Outline each Plasmodium malariae-infected red blood cell.
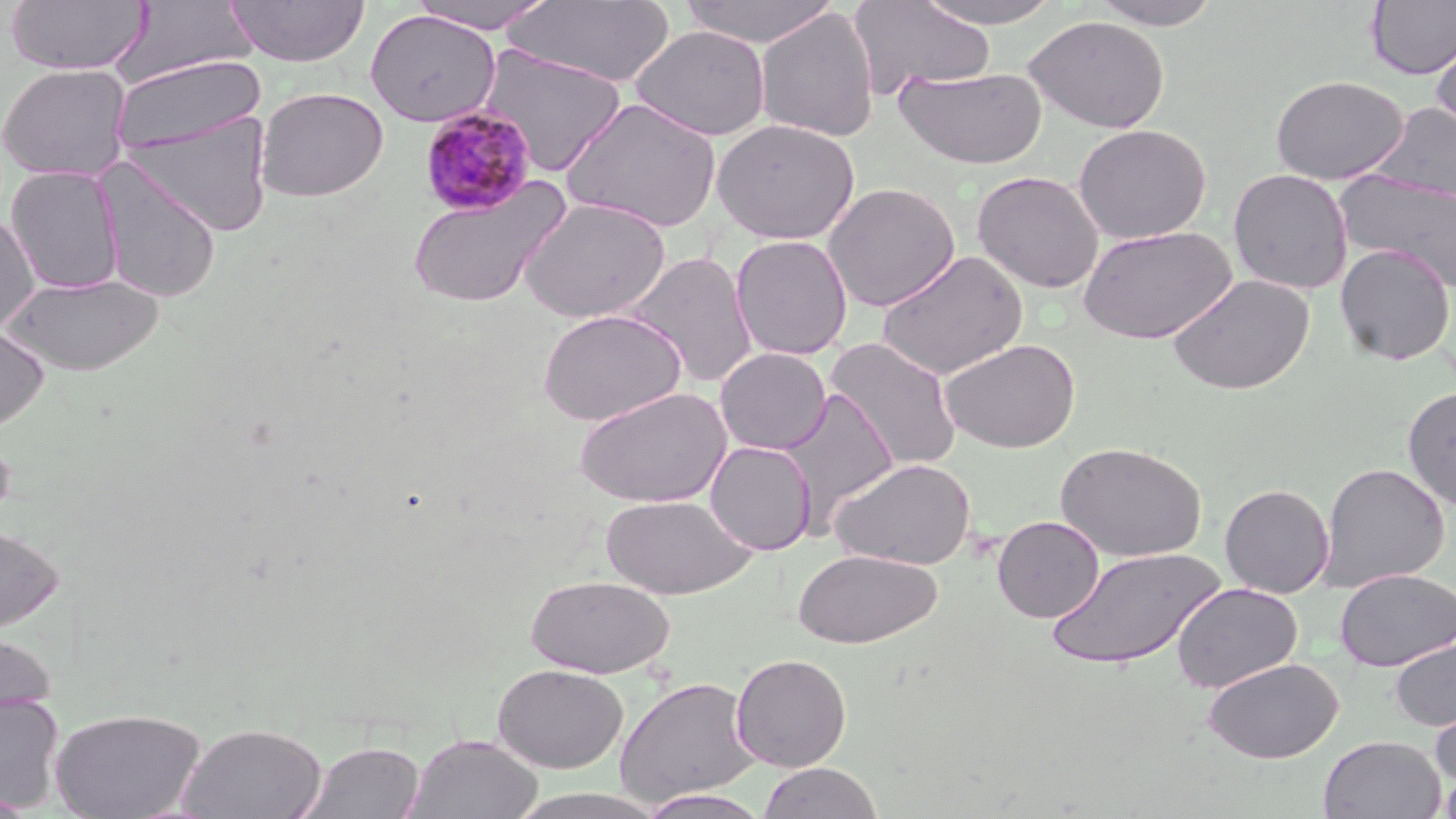

Approximate bounding boxes as (x1, y1, x2, y2) in pixels.
Plasmodium malariae-infected red blood cells: (419, 105, 537, 217).

Summary:
  - Uninfected red blood cell locations: (5, 0, 151, 76), (226, 0, 370, 66), (405, 0, 560, 33), (504, 0, 676, 87), (677, 0, 841, 48), (848, 0, 996, 99), (912, 0, 1068, 28), (1086, 0, 1227, 30), (113, 1, 259, 86), (1365, 1, 1456, 80), (755, 8, 879, 143), (364, 9, 501, 126), (1024, 15, 1170, 133), (1430, 24, 1456, 138), (631, 25, 771, 140), (477, 45, 627, 176), (109, 54, 266, 155), (0, 62, 133, 182), (893, 65, 1046, 169), (1271, 75, 1409, 185), (255, 86, 389, 202), (560, 97, 723, 233), (1372, 102, 1456, 203), (126, 112, 273, 238), (712, 118, 859, 245), (1073, 124, 1211, 244), (95, 158, 222, 304), (5, 165, 125, 294), (1228, 168, 1353, 295), (1335, 170, 1456, 293), (972, 171, 1105, 294), (407, 178, 570, 309), (822, 182, 960, 312), (519, 197, 671, 323), (0, 211, 40, 335), (1078, 225, 1237, 344), (731, 235, 853, 360), (1335, 243, 1455, 366), (877, 249, 1028, 381), (625, 251, 759, 389), (4, 273, 163, 376), (1167, 273, 1315, 396), (537, 308, 686, 426), (0, 322, 50, 434), (825, 336, 963, 471), (939, 337, 1082, 453), (715, 347, 832, 455), (1402, 385, 1456, 510), (574, 386, 733, 508), (776, 386, 898, 531), (0, 430, 16, 528), (705, 441, 817, 555), (1055, 441, 1206, 561), (830, 457, 976, 570), (1319, 462, 1451, 591), (1220, 483, 1335, 598), (600, 494, 756, 600), (992, 515, 1105, 623), (0, 524, 65, 634), (1047, 546, 1224, 669), (792, 548, 943, 649), (1335, 568, 1456, 671), (526, 574, 676, 678), (1172, 582, 1303, 693), (0, 629, 57, 718), (1389, 636, 1456, 733), (730, 653, 852, 771), (1204, 657, 1343, 763), (492, 663, 628, 773), (614, 675, 760, 808), (0, 693, 65, 812), (1429, 700, 1456, 791), (49, 707, 206, 819), (176, 721, 327, 818), (405, 733, 543, 819), (1318, 734, 1447, 819), (296, 739, 427, 819), (757, 761, 884, 819), (1437, 765, 1455, 818), (507, 788, 671, 819), (637, 788, 772, 818), (0, 792, 40, 818)
  - Slide-level diagnosis: Plasmodium malariae
  - Modality: light microscopy
  - Field of view: one of a larger specimen
  - Image size: 1456×819 pixels
  - Preparation: thin blood film
  - Stain: May-Grünwald-Giemsa
  - Magnification: 1000x